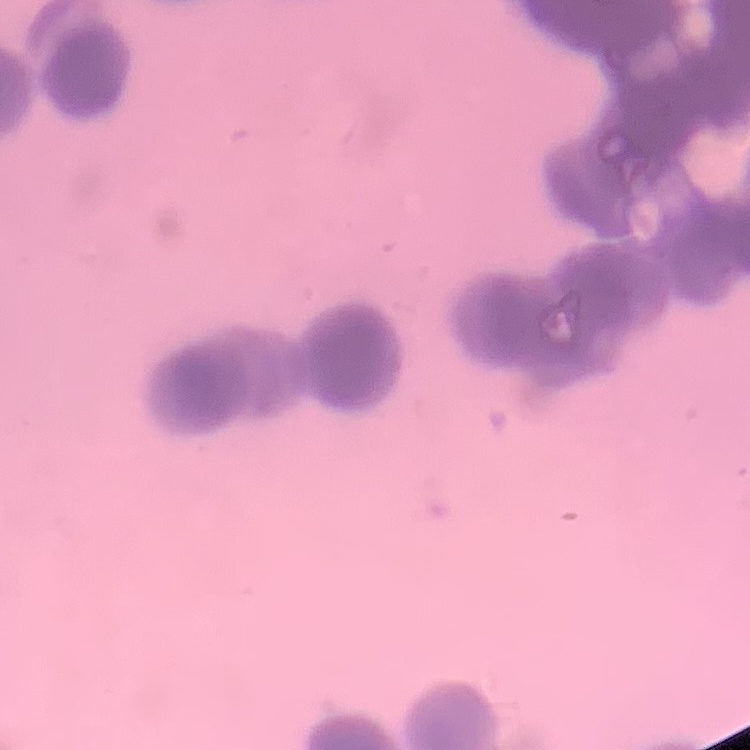
erythrocyte morphology = rouleaux formation
preparation = thin blood smear
image type = square crop of a larger photomicrograph
stain = Field's or Giemsa